Give the position of every leukocyte visible.
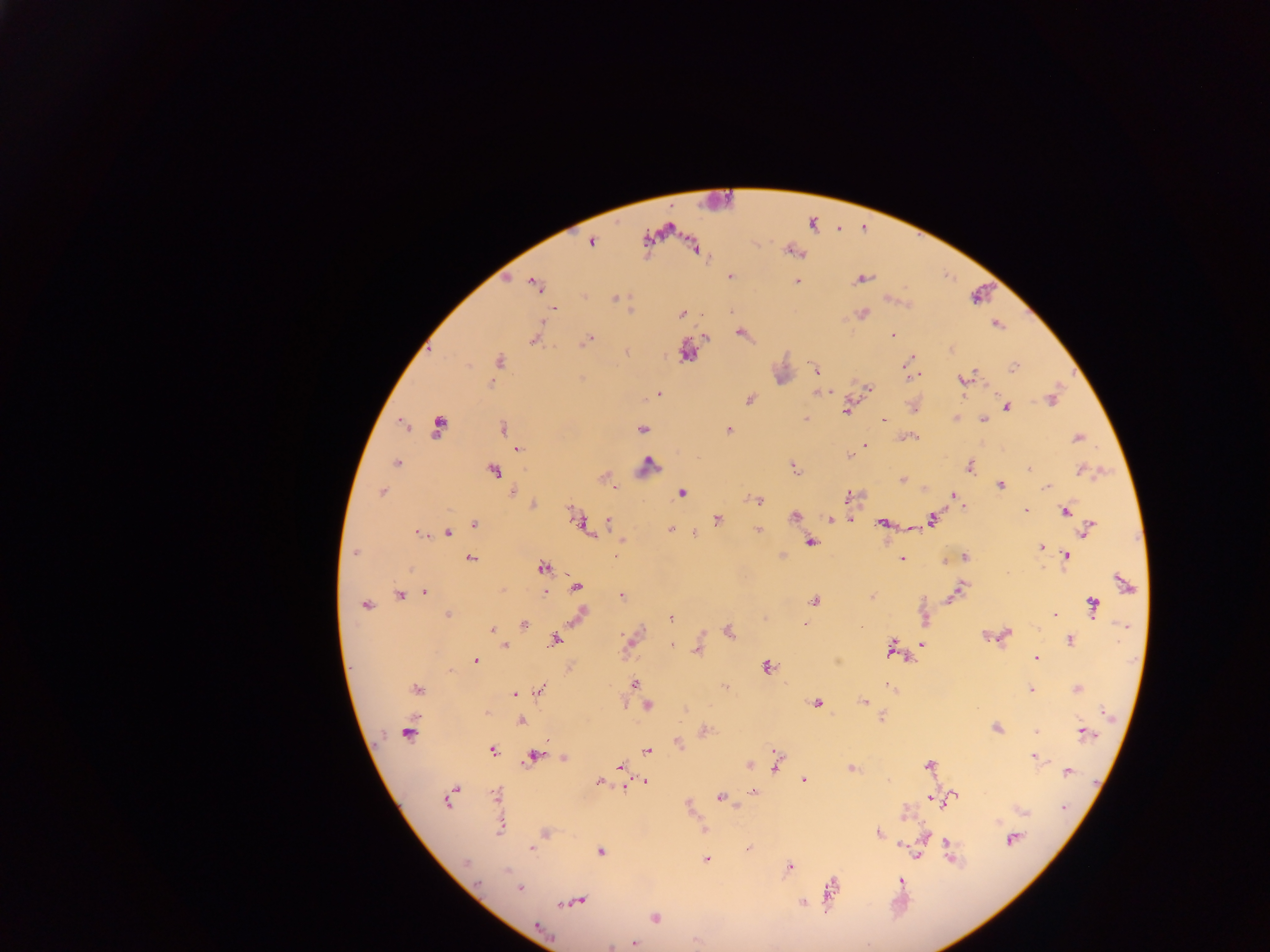

No leukocytes observed.

Approximate centers as [x, y] in pixels. Malaria parasite locations: [591, 242], [694, 247], [793, 250], [730, 276], [861, 279], [795, 280], [534, 284], [583, 296], [614, 297], [553, 308], [861, 313], [681, 314], [996, 324], [741, 333], [892, 336], [535, 337], [705, 337], [586, 341], [950, 348], [684, 351], [908, 360], [498, 361], [1014, 367], [816, 368], [908, 369], [916, 375], [964, 379], [868, 388], [819, 392], [659, 394], [750, 399], [1051, 399], [913, 405], [1005, 407], [846, 410], [957, 418], [806, 419], [883, 419], [982, 419], [402, 425], [438, 426], [503, 429], [642, 429], [729, 430], [906, 437], [1075, 437], [864, 445], [517, 449], [847, 454], [396, 462], [647, 466], [969, 466], [794, 468], [491, 470], [1029, 470], [1082, 470], [605, 477], [902, 480], [1000, 485], [613, 486], [1047, 486], [381, 492], [512, 493], [682, 493], [955, 495], [848, 497], [756, 500], [963, 504], [533, 505], [1065, 510], [1025, 511], [794, 515], [830, 518], [717, 519], [850, 519], [931, 519], [578, 521], [607, 522], [883, 523], [475, 524], [586, 528], [1088, 528], [670, 530], [757, 530], [419, 532], [446, 532], [694, 534], [622, 539], [810, 542], [1041, 547], [355, 553], [1066, 555], [615, 557], [964, 557], [470, 558], [901, 558], [945, 560], [542, 568], [1122, 583], [576, 587], [502, 590], [544, 591], [425, 592], [952, 593], [400, 595], [621, 595], [870, 597], [814, 600], [366, 605], [1093, 606], [447, 614], [581, 614], [1053, 614], [670, 618], [805, 624], [524, 625], [493, 630], [728, 630], [1003, 635], [1069, 639], [555, 640], [629, 641], [921, 644], [670, 645], [504, 646], [892, 646], [698, 647], [1036, 659], [475, 660], [767, 667], [634, 684], [636, 684], [888, 686], [726, 687], [417, 689], [539, 689], [1076, 689], [1031, 690], [515, 693], [864, 701], [816, 702], [647, 704], [486, 710], [1103, 712], [882, 717], [520, 721], [996, 728], [407, 731], [705, 731], [1036, 731], [1083, 732], [677, 742], [493, 750], [647, 751], [534, 756], [563, 757], [1035, 757], [776, 763], [749, 764], [929, 765], [620, 766], [851, 768], [1067, 771], [803, 780], [646, 781], [599, 782], [624, 788], [754, 791], [497, 795], [721, 796], [951, 796], [450, 797], [930, 799], [688, 806], [1063, 807], [1021, 809], [904, 813], [500, 825], [703, 830], [544, 833], [877, 833], [924, 837], [1011, 839], [947, 843], [901, 844], [532, 847], [600, 851], [917, 854], [706, 859], [788, 867], [507, 871], [900, 880], [519, 887], [830, 889], [574, 901], [802, 902], [654, 918], [539, 928], [633, 943]. Image is 1270×952 pixels. Collected in Ghana. Mobile-phone photograph taken through the microscope. Single field of view. Thick blood film.